Locate every Plasmodium vivax-infected red blood cell.
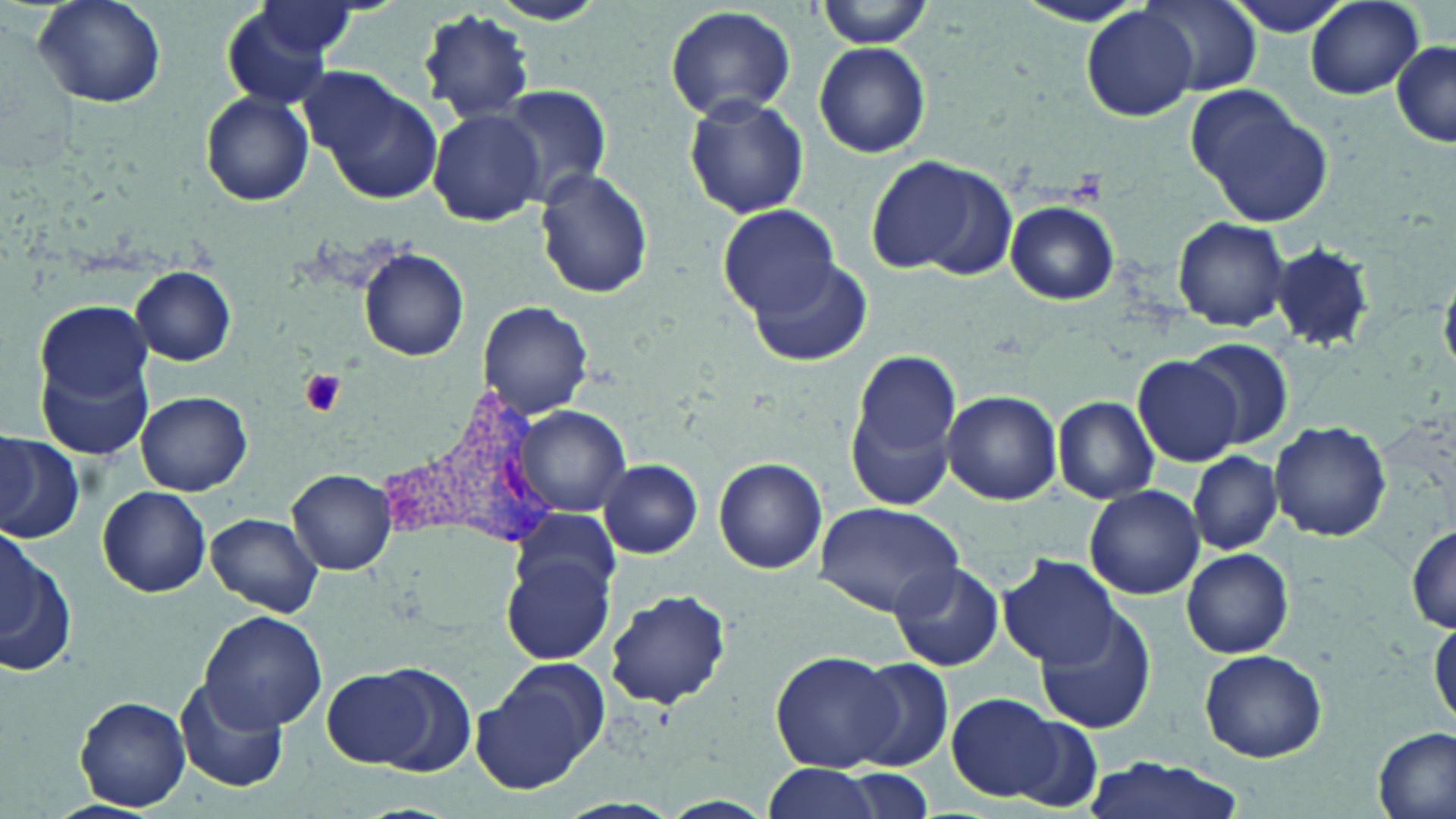
Approximate bounding boxes as [x1, y1, x2, y2] in pixels.
Plasmodium vivax-infected red blood cells: [393, 390, 569, 553].

slide_level_diagnosis: Plasmodium vivax
platelet_locations: 'approximate bounding boxes as [x1, y1, x2, y2] in pixels: [297, 368, 347, 417]'
uninfected_red_blood_cell_locations: 'approximate bounding boxes as [x1, y1, x2, y2] in pixels: [33, 0, 168, 109], [816, 0, 935, 48], [1226, 0, 1355, 39], [1304, 0, 1425, 99], [484, 1, 611, 27], [1142, 1, 1264, 98], [1010, 2, 1152, 29], [664, 4, 797, 122], [221, 5, 343, 110], [252, 5, 359, 55], [1082, 7, 1198, 122], [419, 8, 536, 124], [1391, 40, 1456, 146], [814, 42, 932, 158], [308, 69, 444, 203], [496, 83, 613, 207], [1189, 87, 1334, 227], [201, 91, 313, 205], [683, 93, 809, 219], [428, 108, 544, 225], [866, 156, 999, 275], [535, 170, 654, 298], [1006, 200, 1119, 305], [718, 206, 842, 316], [1170, 215, 1292, 331], [1270, 245, 1376, 353], [358, 247, 469, 361], [746, 254, 870, 367], [131, 267, 236, 365], [35, 298, 153, 414], [479, 300, 591, 419], [1182, 336, 1296, 451], [847, 347, 965, 509], [39, 352, 156, 463], [1134, 354, 1245, 466], [943, 389, 1062, 503], [135, 392, 251, 495], [1053, 395, 1160, 503], [516, 405, 631, 514], [1269, 422, 1391, 541], [0, 432, 84, 544], [1190, 450, 1282, 555], [713, 458, 827, 574], [598, 459, 701, 557], [288, 468, 380, 575], [1084, 485, 1204, 600], [98, 486, 211, 598], [812, 502, 965, 615], [207, 513, 322, 617], [848, 518, 996, 655], [1406, 524, 1456, 633], [0, 528, 76, 680], [1181, 546, 1294, 658], [502, 553, 615, 664], [998, 556, 1123, 671], [891, 562, 1004, 672], [603, 587, 733, 712], [1037, 606, 1156, 734], [199, 609, 328, 732], [1428, 618, 1455, 728], [1199, 648, 1329, 763], [770, 649, 905, 771], [851, 657, 954, 770], [321, 662, 459, 774], [471, 662, 608, 794], [175, 679, 288, 795], [946, 692, 1062, 800], [75, 695, 192, 811], [1008, 715, 1106, 811], [1374, 726, 1453, 819], [1074, 756, 1253, 819], [757, 764, 888, 819], [843, 768, 935, 817]'
image_size: 1456×819 pixels
stain: May-Grünwald-Giemsa
modality: light microscopy
field_of_view: one of a larger specimen
preparation: thin blood film
magnification: 1000x